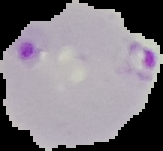

result = Plasmodium parasites identified
image size = 163×151 pixels
image type = segmented cell region with the area outside set to black
preparation = thin blood smear